Name the cell type shown.
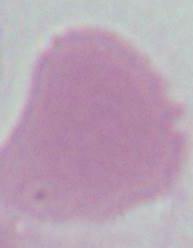
An erythrocyte.

Summary:
  - Modality: micrograph
  - Magnification: 1000x